Classify this cell by malaria status.
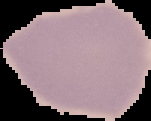

It is uninfected.

image_size: 151×121 pixels
image_type: segmented cell region with the area outside set to black
preparation: thin blood smear